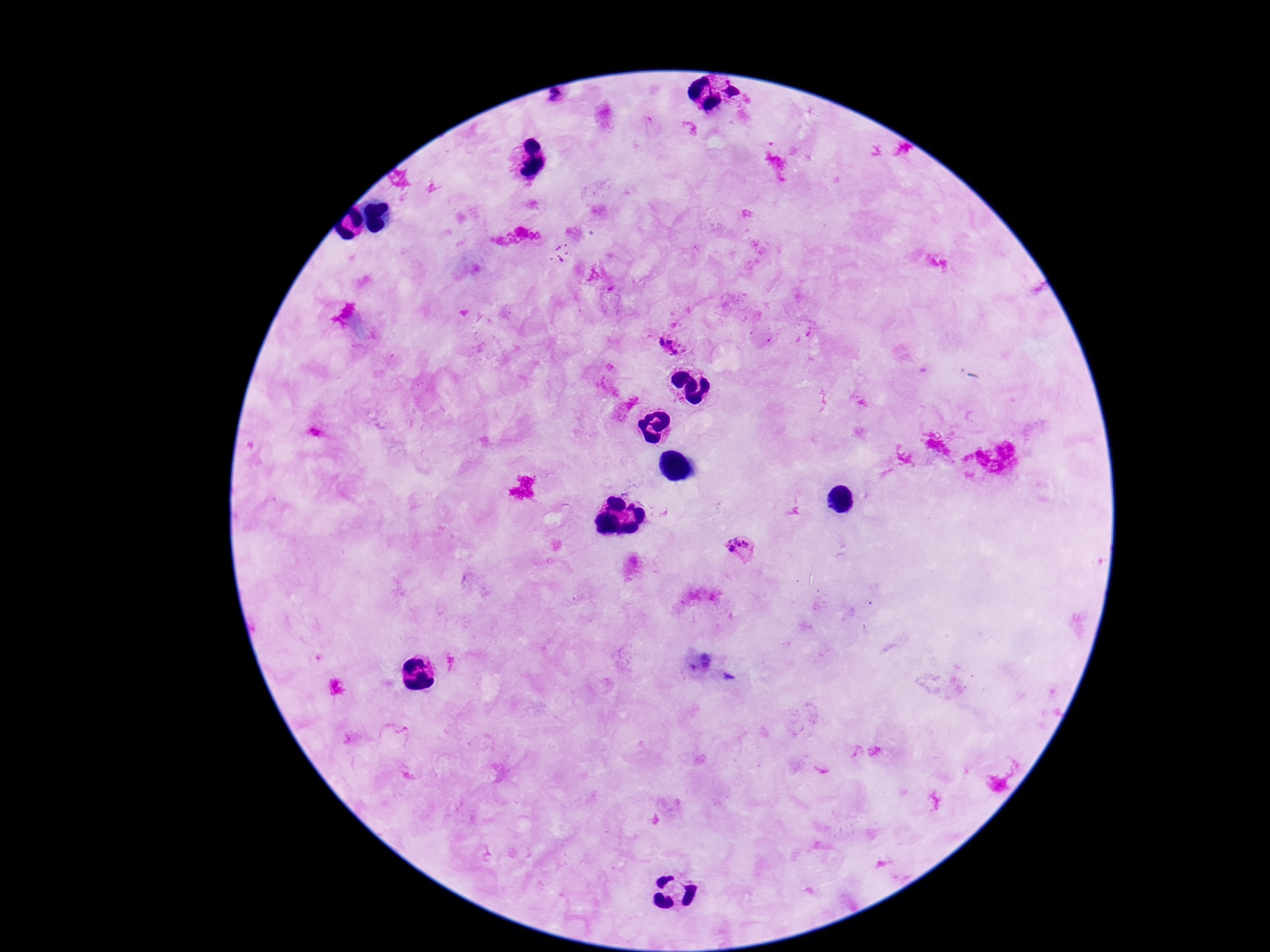

Approximate centers as {x, y} in pixels.
Summary:
  - Plasmodium parasite locations: {558, 99}, {670, 347}, {741, 548}
  - Field of view: single
  - Patient malaria status: positive
  - Magnification: 100x
  - Image size: 1270×952 pixels
  - Stain: Giemsa
  - Capture: smartphone camera through the microscope eyepiece
  - Preparation: thick peripheral-blood smear